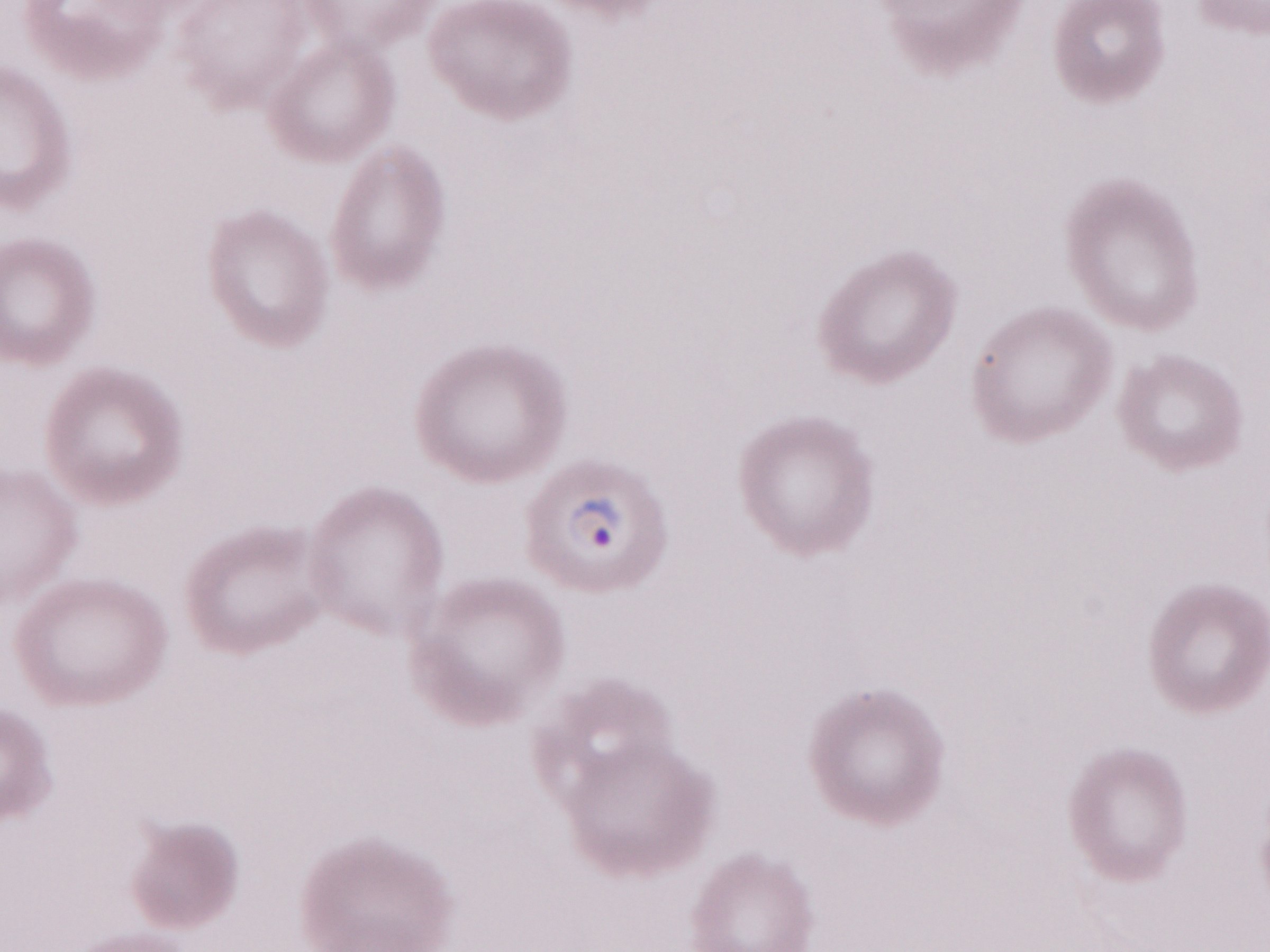 May-Grünwald-Giemsa stain. Malaria diagnosis (patient-level): positive. One field of this slide. Image is 1270×952 pixels. Magnification: 1,000x. Olympus BX43 microscope, Olympus DP73 camera. Thin blood smear.